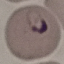
Result: malaria parasites identified. Acquired by smartphone through the microscope eyepiece. Thin smear of blood. Giemsa stain. Automatically extracted cell patch, resized to 64 × 64 pixels.